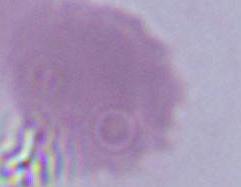 1000x magnification. A red blood cell is shown. Micrograph.